Report the malaria status of this cell.
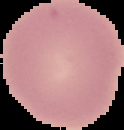

It is uninfected.

Summary:
  - Preparation: thin blood film
  - Image type: segmented cell region with the area outside set to black
  - Image size: 124×130 pixels